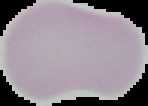
Summary:
  - Image size: 148×106 pixels
  - Image type: cell region segmented out of the field of view; surrounding area masked to black
  - Preparation: thin blood smear
  - Result: no malaria parasites seen